Describe the morphology of the red blood cells.
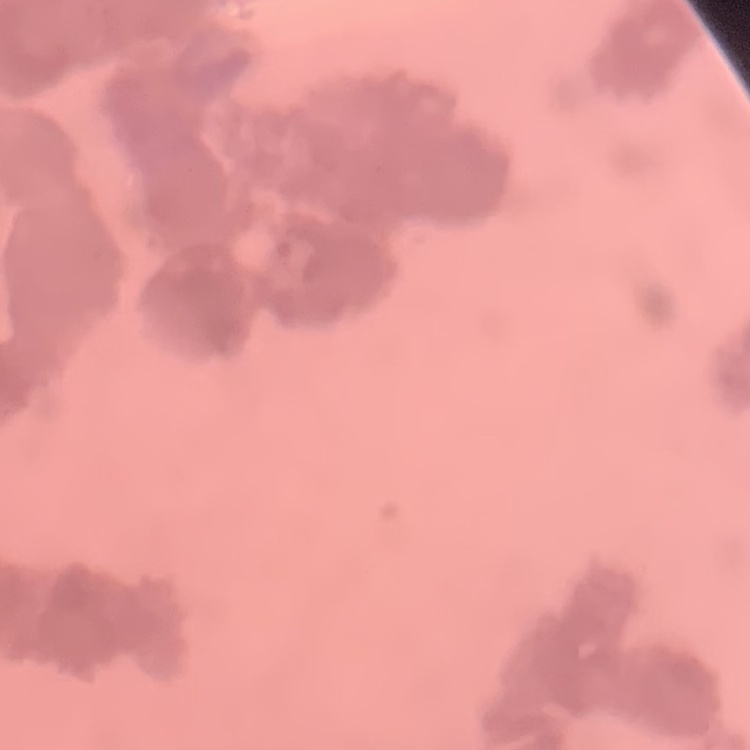
They show rouleaux formation.

Thin blood smear. One tile cut from a larger photomicrograph. Stained with either Field's or Giemsa.